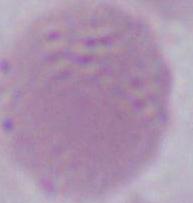

1000x magnification. Micrograph. A red blood cell is seen.